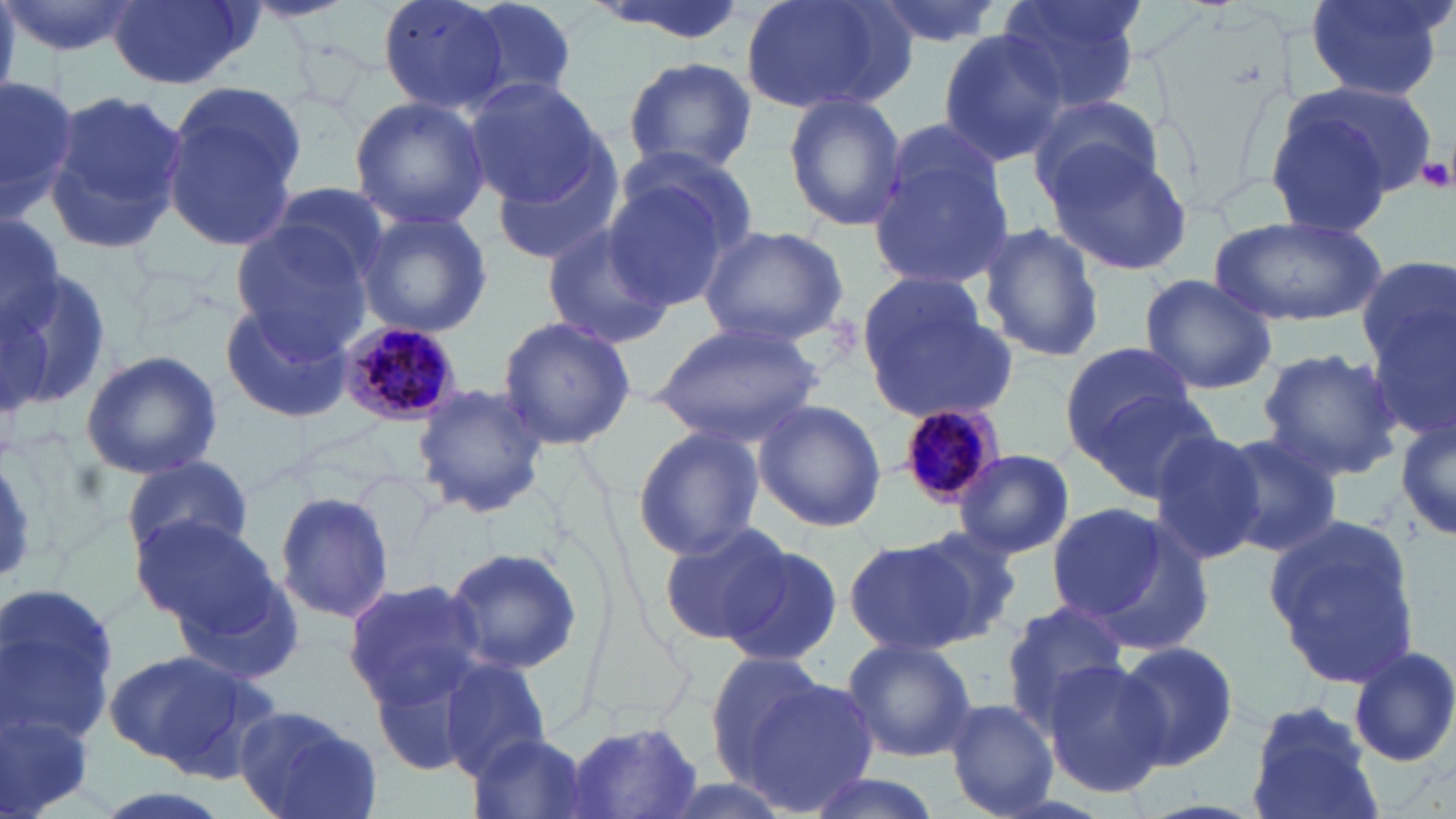
Summary:
  - Coordinate format: approximate bounding boxes as (x1,y1)-(x2,y2) corner pairs in pixels
  - Platelet locations: (1417,156)-(1454,193)
  - Uninfected red blood cell locations: (5,0)-(143,58), (105,0)-(254,91), (244,0)-(359,25), (378,0)-(514,114), (584,0)-(751,44), (738,0)-(914,116), (867,0)-(1004,49), (993,0)-(1148,119), (1304,0)-(1449,99), (457,2)-(582,103), (935,30)-(1068,167), (622,55)-(761,177), (0,72)-(79,217), (464,78)-(607,207), (1290,79)-(1436,201), (159,81)-(307,251), (40,90)-(188,257), (1026,94)-(1164,205), (349,95)-(490,230), (783,95)-(906,231), (1259,99)-(1401,236), (871,129)-(1019,296), (488,141)-(623,267), (1044,142)-(1197,279), (601,168)-(744,311), (263,181)-(394,284), (356,210)-(493,339), (1212,215)-(1383,327), (229,217)-(374,350), (539,222)-(675,348), (979,224)-(1105,363), (696,225)-(850,348), (1355,254)-(1456,393), (5,266)-(114,411), (1136,272)-(1280,393), (857,281)-(1015,423), (220,299)-(350,421), (1367,300)-(1456,447), (496,315)-(635,450), (652,319)-(826,444), (1060,341)-(1197,450), (1256,348)-(1401,482), (80,350)-(224,480), (412,382)-(549,520), (1084,389)-(1221,503), (752,399)-(886,533), (1398,416)-(1455,543), (631,425)-(764,560), (1148,428)-(1269,567), (1214,431)-(1347,557), (955,449)-(1075,561), (120,455)-(255,563), (0,458)-(44,584), (274,488)-(394,622), (1044,501)-(1197,637), (1260,512)-(1425,690), (130,514)-(288,645), (656,522)-(788,646), (905,525)-(1023,641), (844,533)-(991,654), (717,539)-(843,669), (441,545)-(585,676), (342,579)-(491,709), (0,585)-(118,759), (998,598)-(1128,732), (837,636)-(979,765), (1116,640)-(1239,770), (1348,647)-(1456,768), (103,651)-(278,777), (703,651)-(844,783), (437,658)-(554,782), (1041,658)-(1169,796), (735,678)-(879,814), (943,697)-(1059,815), (1243,698)-(1384,819), (231,705)-(380,819), (1,707)-(99,819), (566,720)-(706,817), (464,734)-(603,819), (800,773)-(946,819), (89,788)-(237,819)
  - Plasmodium malariae-infected red blood cell locations: (333,322)-(463,428), (892,404)-(1002,508)
  - Slide-level diagnosis: Plasmodium malariae
  - Stain: May-Grünwald-Giemsa
  - Magnification: 1000x
  - Preparation: thin blood film
  - Field of view: single
  - Image size: 1456×819 pixels
  - Modality: optical microscopy